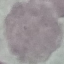

{
  "malaria_status": "uninfected",
  "preparation": "thin blood smear",
  "image_type": "cell patch, automatically extracted from a larger field of view and resized to 64 × 64 pixels",
  "stain": "Giemsa",
  "capture": "smartphone through the microscope eyepiece"
}